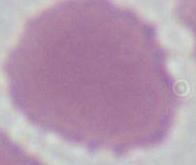
identification = erythrocyte
modality = micrograph
magnification = 1000x